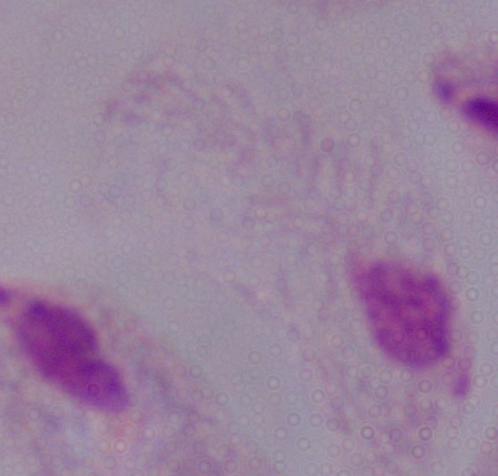
Summary:
  - Magnification: 1000x
  - Modality: micrograph
  - Identification: trichomonad